Assess the morphology of the erythrocytes.
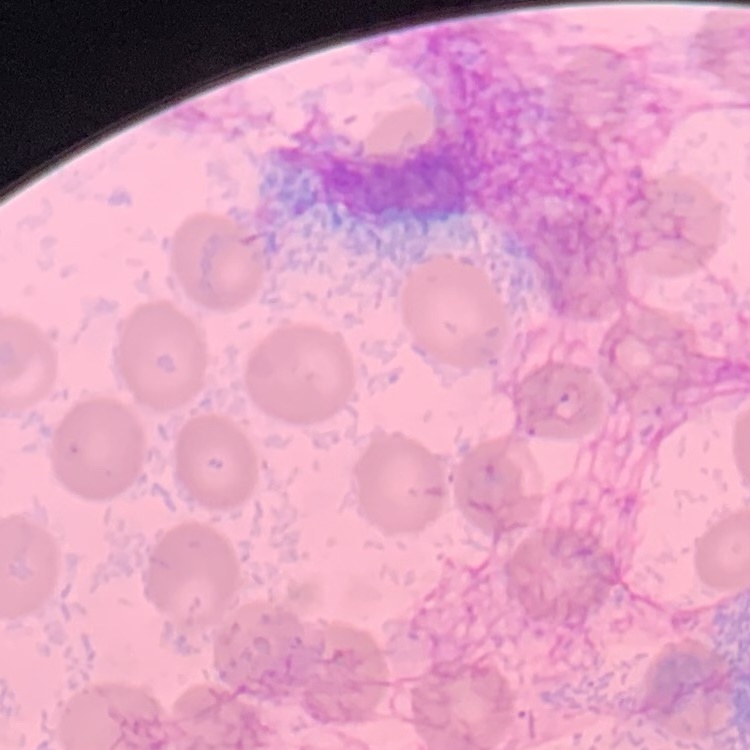

They show no rouleaux formation.

Summary:
  - Stain: Field's or Giemsa
  - Image type: one tile cut from a larger photomicrograph
  - Preparation: thin blood smear